Give the extent of all Plasmodium falciparum-infected red blood cells.
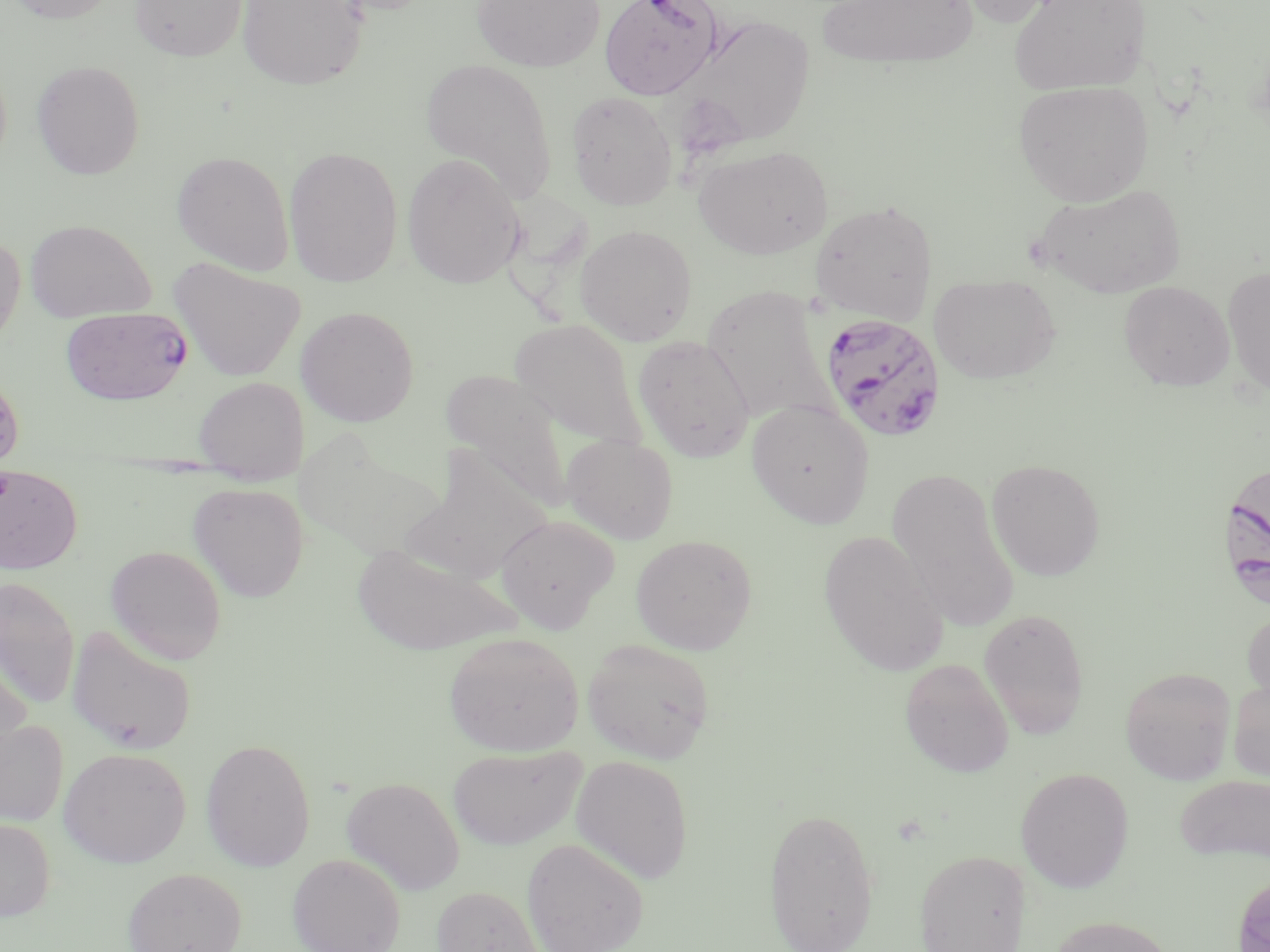
Approximate bounding boxes as named x1/y1/x2/y2 corners in pixels.
Plasmodium falciparum-infected red blood cells: (x1=599, y1=0, x2=723, y2=100), (x1=60, y1=307, x2=193, y2=405), (x1=818, y1=313, x2=947, y2=442), (x1=1222, y1=457, x2=1270, y2=602).

{
  "slide_level_diagnosis": "Plasmodium falciparum",
  "magnification": "1000x",
  "preparation": "thin blood film",
  "image_size": "1270×952 pixels",
  "stain": "May-Grünwald-Giemsa",
  "uninfected_red_blood_cell_locations": "approximate bounding boxes as named x1/y1/x2/y2 corners in pixels: (x1=5, y1=0, x2=121, y2=24), (x1=129, y1=0, x2=248, y2=61), (x1=237, y1=0, x2=368, y2=90), (x1=471, y1=0, x2=605, y2=72), (x1=816, y1=0, x2=980, y2=70), (x1=950, y1=0, x2=1068, y2=28), (x1=1009, y1=0, x2=1150, y2=95), (x1=672, y1=13, x2=816, y2=153), (x1=420, y1=57, x2=558, y2=203), (x1=31, y1=60, x2=146, y2=179), (x1=1013, y1=80, x2=1153, y2=206), (x1=566, y1=90, x2=678, y2=210), (x1=693, y1=144, x2=833, y2=259), (x1=284, y1=145, x2=403, y2=287), (x1=171, y1=150, x2=295, y2=275), (x1=402, y1=153, x2=527, y2=289), (x1=1032, y1=183, x2=1187, y2=298), (x1=810, y1=200, x2=938, y2=323), (x1=25, y1=218, x2=155, y2=322), (x1=575, y1=224, x2=698, y2=346), (x1=0, y1=230, x2=25, y2=353), (x1=168, y1=256, x2=307, y2=383), (x1=1222, y1=266, x2=1270, y2=398), (x1=931, y1=273, x2=1062, y2=384), (x1=1119, y1=281, x2=1235, y2=391), (x1=702, y1=284, x2=836, y2=425), (x1=296, y1=305, x2=419, y2=427), (x1=510, y1=319, x2=647, y2=449), (x1=633, y1=334, x2=755, y2=462), (x1=443, y1=369, x2=575, y2=511), (x1=0, y1=370, x2=24, y2=470), (x1=193, y1=376, x2=308, y2=482), (x1=747, y1=400, x2=875, y2=528), (x1=561, y1=433, x2=679, y2=544), (x1=986, y1=458, x2=1106, y2=580), (x1=0, y1=465, x2=83, y2=574), (x1=887, y1=468, x2=1018, y2=627), (x1=188, y1=482, x2=309, y2=602), (x1=495, y1=515, x2=620, y2=634), (x1=818, y1=530, x2=949, y2=676), (x1=631, y1=534, x2=758, y2=655), (x1=350, y1=542, x2=519, y2=656), (x1=105, y1=545, x2=227, y2=664), (x1=0, y1=577, x2=80, y2=708), (x1=1241, y1=605, x2=1270, y2=714), (x1=978, y1=607, x2=1090, y2=739), (x1=66, y1=626, x2=197, y2=755), (x1=444, y1=632, x2=584, y2=756), (x1=582, y1=638, x2=715, y2=763), (x1=0, y1=652, x2=32, y2=771), (x1=899, y1=658, x2=1014, y2=778), (x1=1119, y1=666, x2=1237, y2=785), (x1=1228, y1=674, x2=1270, y2=784), (x1=0, y1=720, x2=69, y2=827), (x1=200, y1=739, x2=316, y2=871), (x1=448, y1=745, x2=586, y2=850), (x1=59, y1=746, x2=191, y2=868), (x1=571, y1=755, x2=694, y2=884), (x1=1016, y1=767, x2=1135, y2=892), (x1=1175, y1=773, x2=1270, y2=865), (x1=341, y1=777, x2=465, y2=896), (x1=763, y1=805, x2=880, y2=952), (x1=0, y1=817, x2=55, y2=922), (x1=522, y1=838, x2=649, y2=952), (x1=914, y1=849, x2=1028, y2=952), (x1=287, y1=853, x2=406, y2=952), (x1=122, y1=867, x2=247, y2=952), (x1=1231, y1=870, x2=1270, y2=951), (x1=430, y1=885, x2=545, y2=952), (x1=1045, y1=914, x2=1180, y2=952)",
  "modality": "light microscopy",
  "field_of_view": "one of a larger specimen"
}